Name the parasite shown.
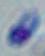

This is Toxoplasma gondii.

Micrograph. Captured at 1000x magnification.